Outline each blood parasite and name the species.
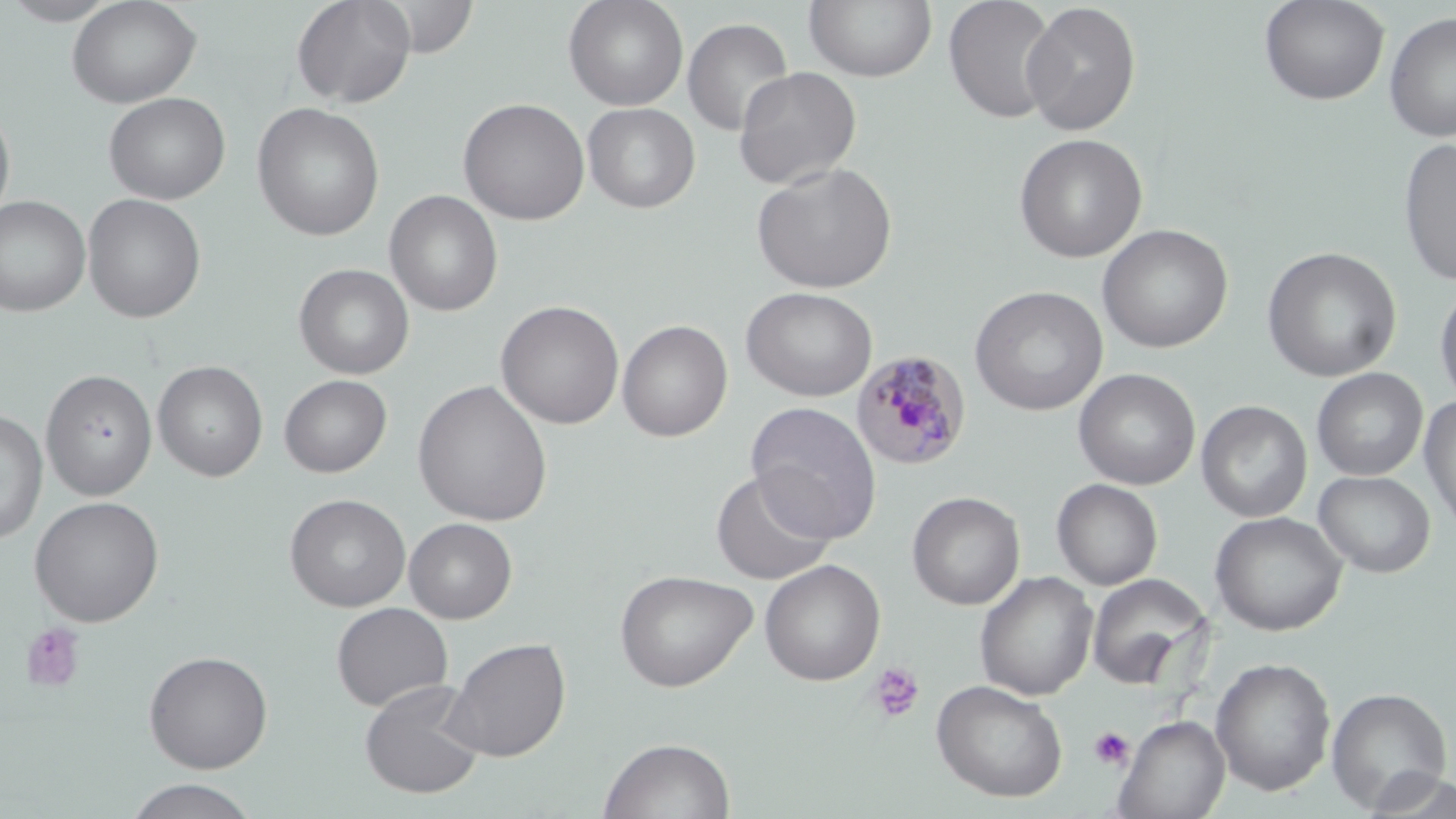
Approximate bounding boxes as (x1, y1, x2, y2) in pixels.
Plasmodium malariae-infected red blood cells: (850, 350, 972, 471).
No Plasmodium falciparum, Plasmodium ovale, Plasmodium vivax, Babesia divergens, or Trypanosoma brucei observed.

Summary:
  - Uninfected red blood cell locations: (2, 0, 121, 25), (67, 0, 202, 108), (290, 0, 416, 109), (373, 0, 480, 58), (563, 0, 689, 110), (943, 0, 1058, 123), (1259, 0, 1390, 106), (804, 1, 937, 83), (1021, 1, 1141, 136), (1384, 11, 1456, 142), (682, 17, 793, 137), (733, 66, 861, 190), (103, 91, 230, 205), (458, 97, 590, 225), (0, 100, 16, 229), (252, 102, 385, 241), (582, 102, 700, 213), (1013, 133, 1148, 263), (1398, 137, 1456, 287), (751, 162, 898, 294), (385, 190, 503, 316), (82, 193, 206, 323), (0, 195, 91, 317), (1097, 224, 1233, 353), (1262, 246, 1402, 382), (294, 263, 414, 379), (1434, 281, 1456, 411), (741, 286, 878, 402), (970, 286, 1108, 416), (496, 300, 624, 429), (617, 319, 733, 442), (153, 361, 268, 482), (1073, 368, 1201, 490), (1312, 368, 1428, 481), (41, 369, 157, 501), (279, 374, 392, 478), (412, 379, 553, 526), (1419, 394, 1456, 534), (1196, 400, 1312, 523), (745, 401, 882, 543), (0, 409, 47, 545), (711, 469, 836, 585), (1313, 470, 1435, 578), (1052, 478, 1163, 590), (907, 490, 1025, 610), (285, 493, 411, 612), (29, 496, 165, 627), (1210, 511, 1347, 636), (404, 517, 517, 623), (759, 559, 886, 686), (615, 569, 757, 692), (975, 571, 1098, 701), (1087, 574, 1213, 692), (331, 602, 453, 711), (442, 636, 571, 762), (143, 649, 273, 773), (1210, 657, 1336, 796), (931, 679, 1068, 802), (359, 680, 485, 799), (1326, 687, 1452, 812), (1114, 714, 1229, 819), (598, 736, 736, 819), (1361, 769, 1456, 818), (124, 778, 260, 818)
  - Platelet locations: (21, 622, 87, 693), (868, 663, 925, 724), (1088, 726, 1135, 770)
  - Slide-level diagnosis: Plasmodium malariae
  - Modality: light microscopy
  - Stain: May-Grünwald-Giemsa
  - Preparation: thin blood smear
  - Image size: 1456×819 pixels
  - Field of view: one of a larger specimen
  - Magnification: 1000x